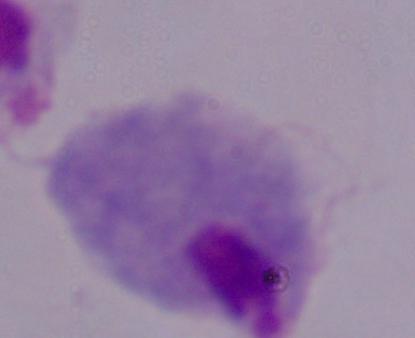
modality = micrograph
identification = trichomonad
magnification = 1000x